Assess the morphology of the red blood cells.
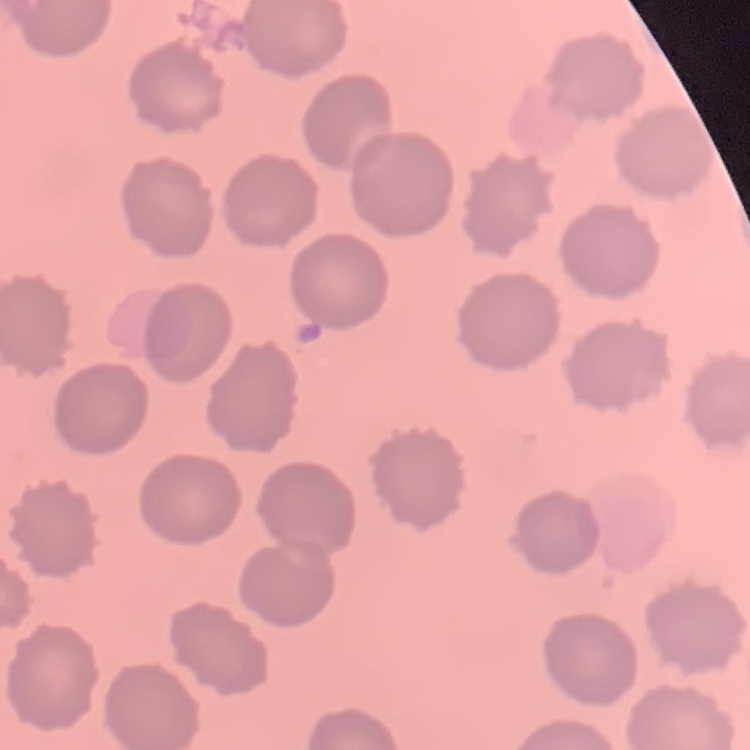
They show no rouleaux formation.

Field's or Giemsa stain. Square crop of a larger photomicrograph. Thin blood film.